State the preparation type.
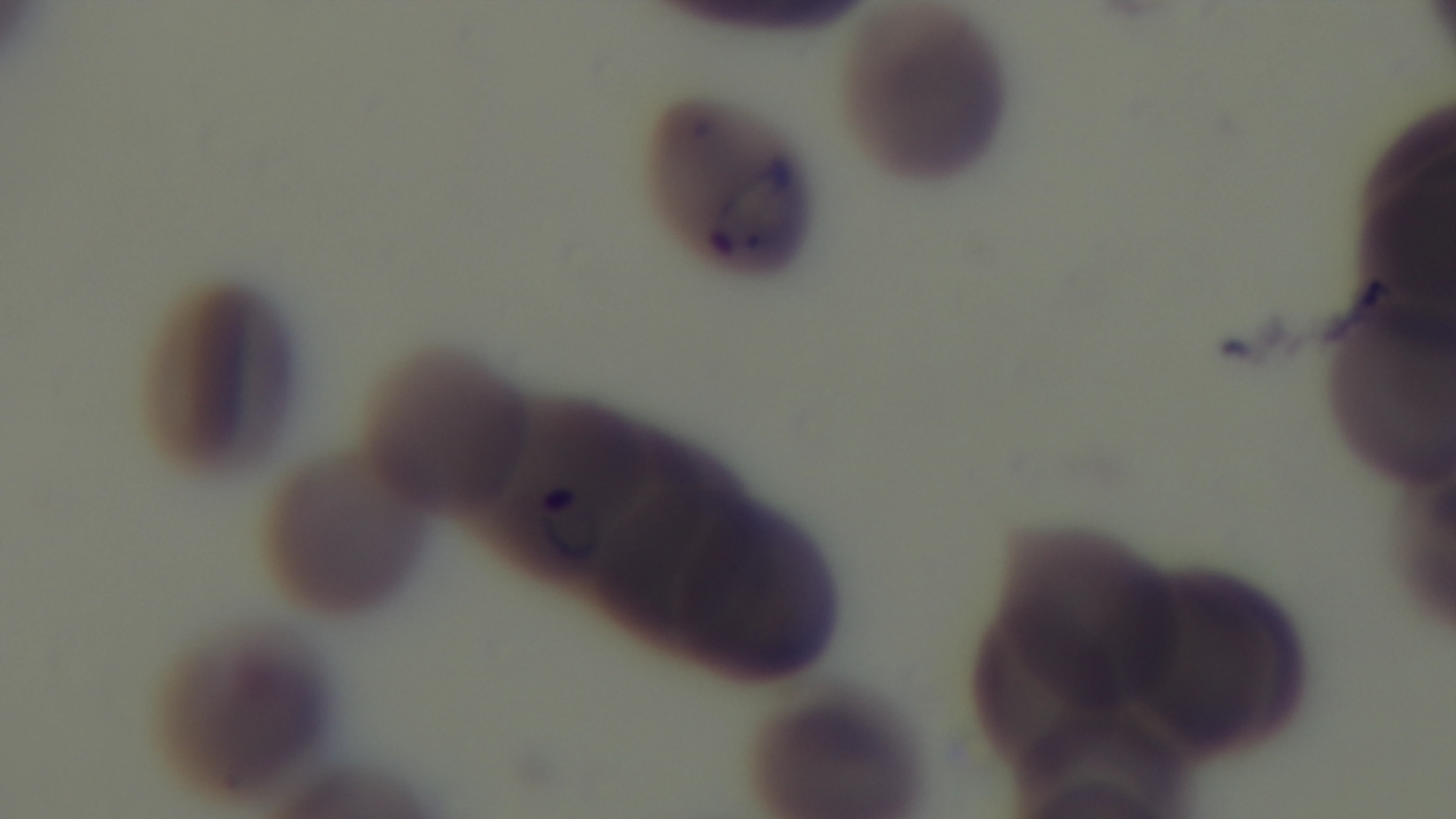

A thin smear.

Summary:
  - Modality: light microscopy
  - Stain: Giemsa
  - Malaria status: positive
  - Objective: 100x oil immersion
  - Field of view: one from the slide
  - Capture: mounted 4K digital camera